Comment on the morphology of the erythrocytes.
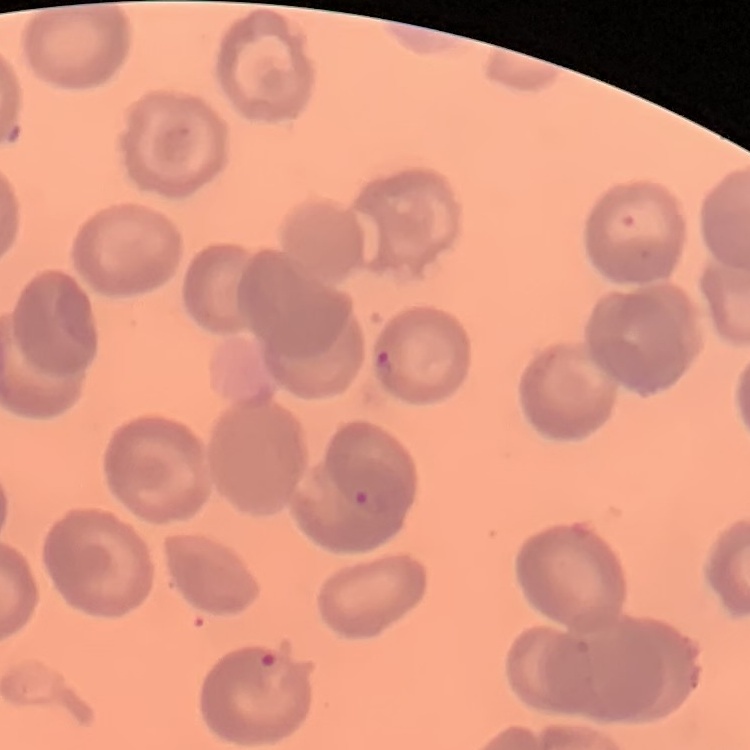
No rouleaux formation.

Square crop of a larger photomicrograph. Thin blood film. Stained with either Field's or Giemsa.